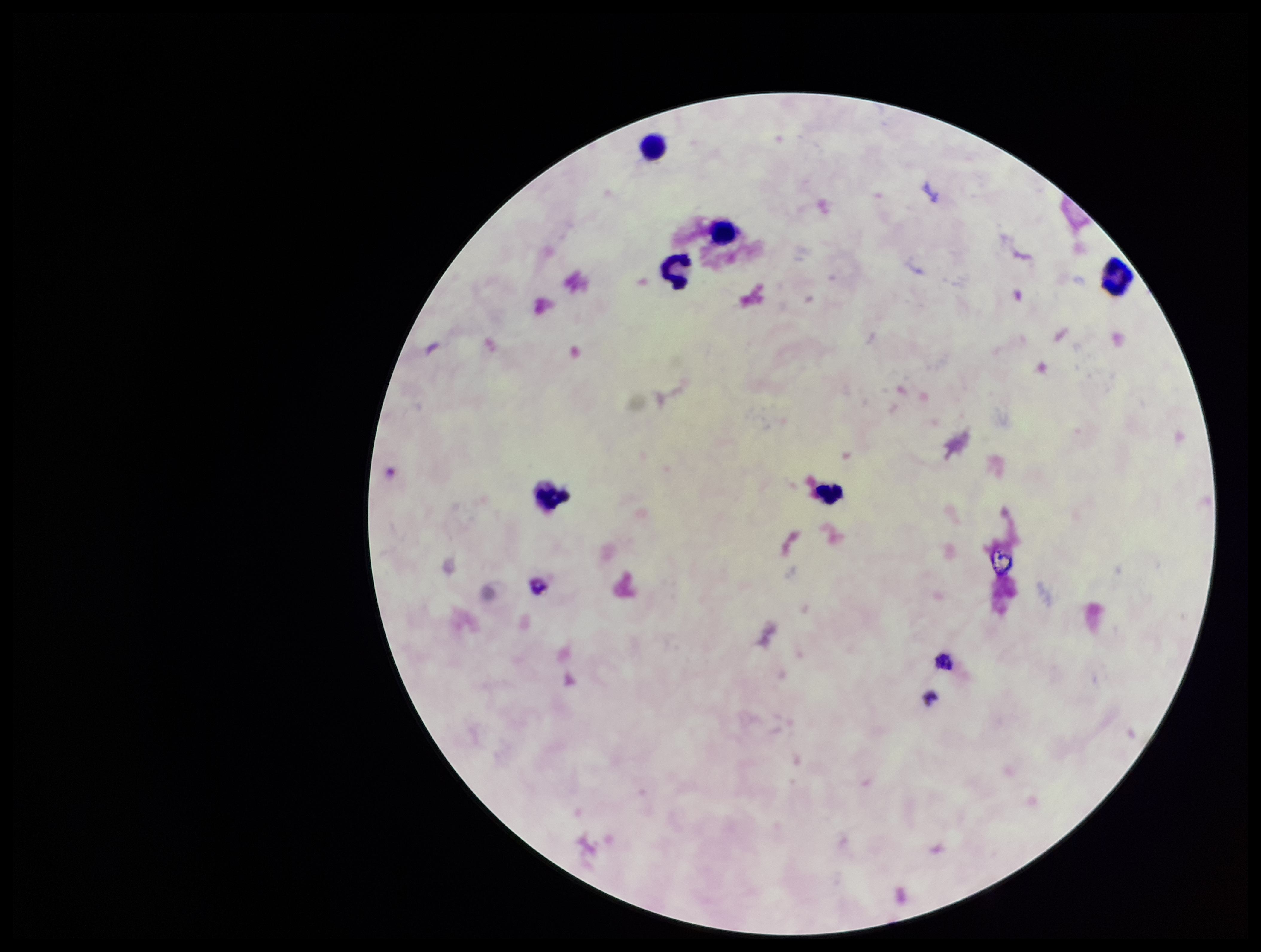
Summary:
  - Parasite count: 0
  - Plasmodium parasites: none identified
  - Capture: smartphone photograph through the microscope eyepiece
  - Preparation: thick smear
  - Image size: 1261×952 pixels
  - Patient malaria status: negative
  - Stain: Giemsa
  - Leukocyte count: 5
  - Field of view: one from this slide